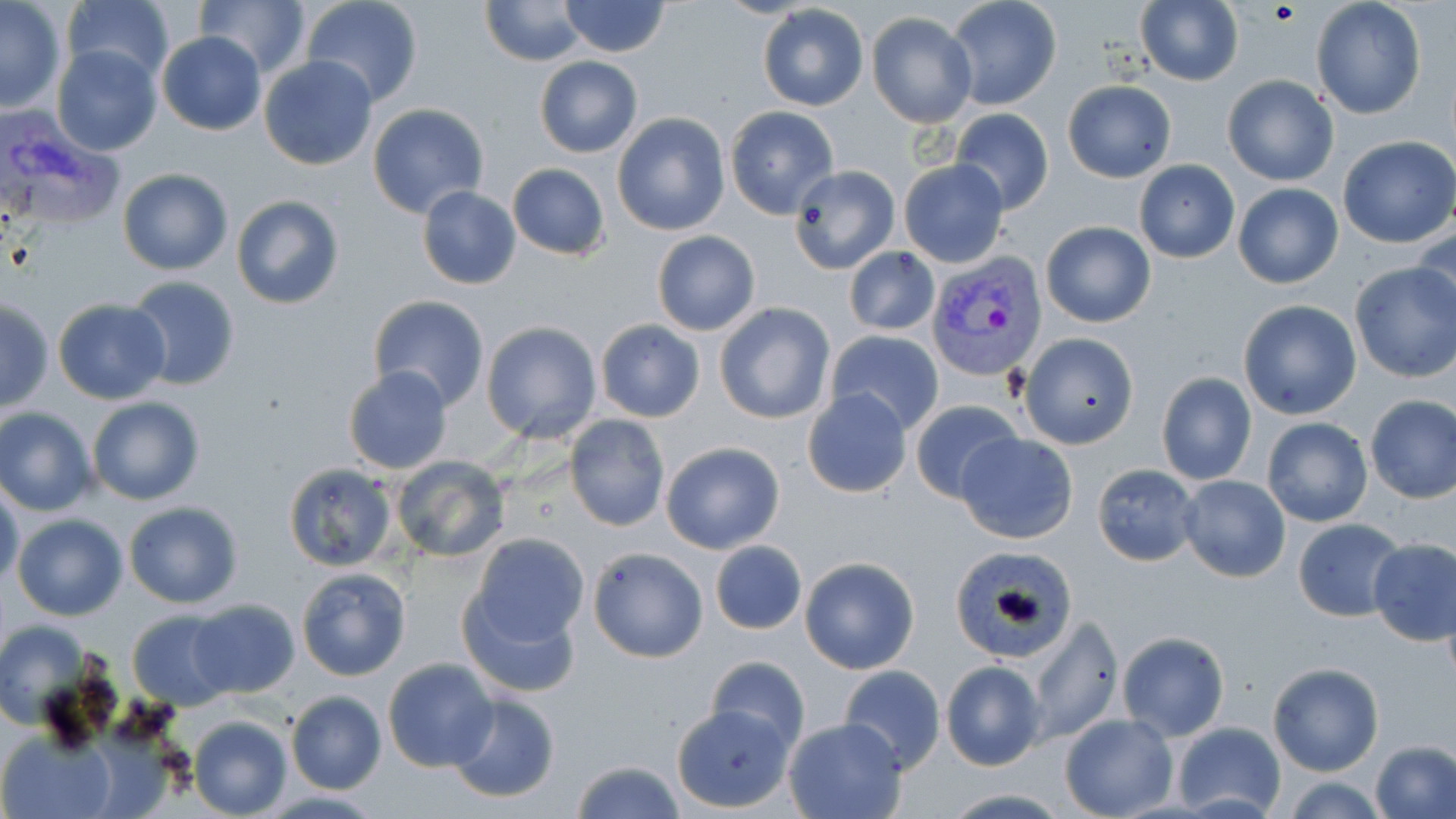

Approximate bounding boxes as [x1, y1, x2, y2] in pixels. Uninfected red blood cell locations: [194, 0, 309, 76], [300, 0, 423, 107], [482, 0, 587, 66], [1310, 0, 1427, 120], [558, 1, 671, 57], [947, 1, 1060, 108], [0, 2, 67, 112], [64, 2, 173, 85], [756, 3, 870, 111], [1134, 3, 1243, 86], [867, 12, 976, 127], [156, 31, 267, 135], [52, 44, 161, 156], [259, 56, 378, 170], [534, 56, 642, 157], [1221, 74, 1340, 186], [1062, 80, 1176, 182], [368, 104, 490, 218], [724, 106, 839, 217], [949, 108, 1053, 216], [613, 112, 729, 236], [1337, 136, 1456, 248], [899, 159, 1009, 268], [1134, 160, 1239, 263], [507, 163, 611, 261], [789, 164, 901, 274], [116, 169, 232, 275], [1232, 183, 1344, 289], [416, 185, 523, 290], [230, 195, 345, 311], [1039, 220, 1157, 327], [1412, 227, 1455, 327], [652, 230, 761, 336], [844, 246, 940, 336], [1349, 262, 1456, 382], [124, 275, 241, 391], [368, 295, 490, 414], [51, 297, 171, 405], [1, 300, 53, 413], [1237, 300, 1360, 420], [715, 302, 835, 424], [595, 319, 705, 422], [481, 321, 602, 443], [826, 329, 943, 435], [1018, 332, 1139, 449], [341, 367, 453, 476], [1156, 372, 1256, 487], [802, 388, 914, 498], [1364, 395, 1456, 503], [87, 396, 206, 506], [909, 398, 1024, 503], [0, 406, 98, 514], [564, 414, 671, 532], [1262, 417, 1372, 527], [955, 433, 1079, 544], [660, 441, 785, 554], [389, 454, 510, 563], [1092, 463, 1201, 566], [282, 464, 397, 570], [1178, 475, 1290, 583], [0, 483, 23, 590], [123, 501, 244, 608], [11, 514, 128, 621], [1292, 517, 1407, 620], [469, 532, 590, 649], [1369, 540, 1456, 646], [710, 541, 807, 634], [588, 546, 709, 663], [949, 549, 1081, 659], [799, 557, 921, 675], [295, 567, 411, 681], [457, 583, 585, 700], [188, 600, 298, 698], [128, 610, 237, 709], [1027, 618, 1122, 743], [0, 619, 88, 728], [1117, 631, 1229, 741], [706, 656, 810, 752], [383, 658, 500, 772], [940, 660, 1045, 770], [1268, 662, 1383, 776], [838, 665, 945, 773], [285, 690, 387, 795], [445, 692, 561, 804], [672, 706, 793, 812], [1060, 713, 1178, 819], [189, 715, 293, 819], [783, 717, 907, 819], [1172, 721, 1286, 816], [2, 732, 115, 818], [1371, 740, 1456, 818], [569, 760, 689, 818], [1283, 777, 1389, 817], [937, 789, 1074, 818]. Plasmodium vivax-infected red blood cell locations: [2, 110, 126, 231], [928, 252, 1047, 383]. Slide-level diagnosis: Plasmodium vivax. One field of a larger specimen. Optical microscopy. May-Grünwald-Giemsa stain. Image is 1456×819 pixels. Thin blood film. 1000x magnification.